Classify this cell by malaria status.
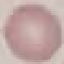
Uninfected.

Acquired by smartphone through the microscope eyepiece. Automatically extracted cell patch, resized to 64 × 64 pixels. Giemsa-stained preparation. Thin blood smear.